Identify the parasite.
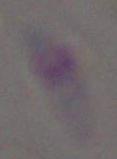
This is Toxoplasma gondii.

magnification = 1000x
modality = photomicrograph